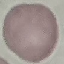

malaria status = uninfected
stain = Giemsa
image type = automatically extracted cell patch, resized to 64 × 64 pixels
preparation = thin blood smear
capture = smartphone through the microscope eyepiece